Report the malaria status of this cell.
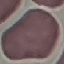

Uninfected.

Summary:
  - Image type: cell patch, automatically extracted from a larger field of view and resized to 64 × 64 pixels
  - Capture: smartphone camera at the microscope eyepiece
  - Preparation: thin blood smear
  - Stain: Giemsa